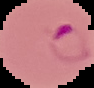
Image is 94×88 pixels. From a thin blood film. Result: malaria parasites detected. The area outside the segmented cell region is set to black.